Identify the blood parasite species.
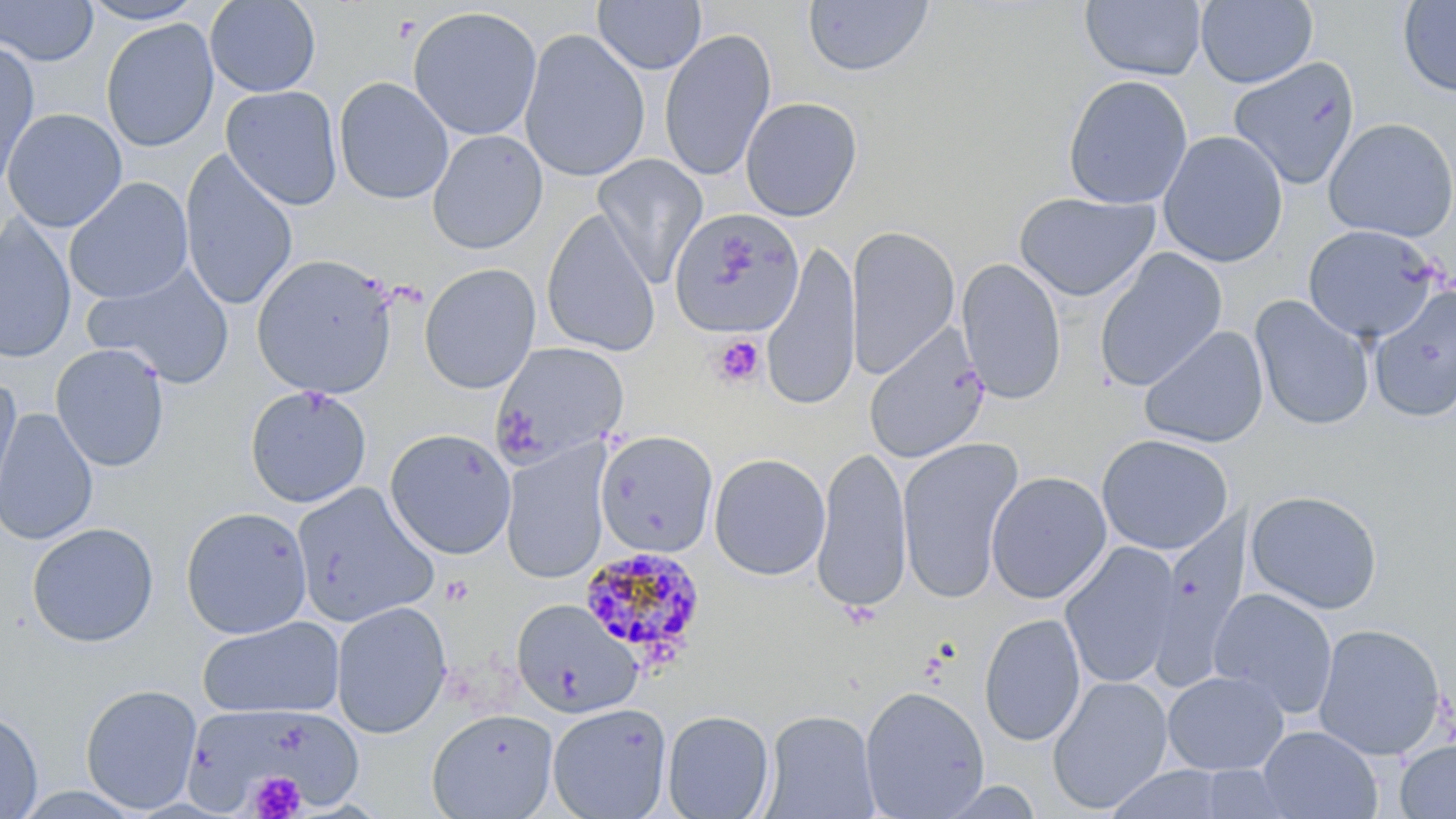
Plasmodium malariae.

Approximate bounding boxes as (x1,y1)-(x2,y2) corner pairs in pixels. Platelet locations: (712,334)-(766,387), (248,770)-(305,818). Uninfected red blood cell locations: (1,0)-(98,66), (77,0)-(207,25), (204,0)-(321,98), (593,0)-(707,74), (1079,0)-(1207,81), (1195,0)-(1318,89), (1397,0)-(1456,98), (802,1)-(934,78), (407,6)-(543,141), (100,18)-(219,153), (518,27)-(650,183), (658,28)-(777,182), (0,39)-(40,188), (1228,56)-(1361,190), (1062,74)-(1193,209), (334,76)-(454,205), (221,85)-(342,211), (740,96)-(863,221), (2,106)-(107,356), (2,108)-(127,232), (1322,117)-(1456,242), (427,130)-(548,254), (1157,130)-(1289,268), (179,150)-(298,312), (592,154)-(708,287), (64,177)-(193,304), (1014,191)-(1159,302), (668,207)-(805,339), (541,209)-(660,357), (1,217)-(76,364), (1302,224)-(1441,342), (845,226)-(960,378), (761,244)-(861,411), (1093,248)-(1228,392), (251,252)-(399,399), (956,257)-(1067,404), (83,263)-(236,391), (418,263)-(541,394), (1368,286)-(1456,423), (1249,295)-(1375,431), (1139,325)-(1269,449), (865,326)-(990,464), (492,342)-(630,464), (50,344)-(170,472), (0,380)-(23,510), (244,386)-(372,508), (0,409)-(99,545), (384,428)-(516,560), (595,430)-(718,558), (1096,433)-(1234,555), (896,438)-(1023,603), (501,441)-(612,585), (811,444)-(913,614), (708,452)-(831,581), (986,471)-(1112,604), (291,481)-(439,628), (1245,489)-(1383,614), (180,506)-(313,639), (1152,513)-(1252,684), (26,522)-(159,647), (1059,541)-(1182,690), (1208,587)-(1339,719), (511,599)-(641,719), (331,601)-(452,738), (978,612)-(1086,747), (197,616)-(344,719), (1313,622)-(1447,761), (1162,670)-(1289,776), (1047,675)-(1173,814), (80,683)-(203,814), (858,685)-(990,817), (185,701)-(359,813), (547,702)-(673,819), (0,707)-(43,819), (426,708)-(559,819), (662,709)-(775,819), (762,709)-(880,818), (1257,726)-(1382,818), (1395,739)-(1456,818). Plasmodium malariae-infected red blood cell locations: (578,545)-(707,668). Thin blood film. May-Grünwald-Giemsa stain. Light microscopy. Single field of view. Captured at 1000x magnification. Image is 1456×819 pixels.